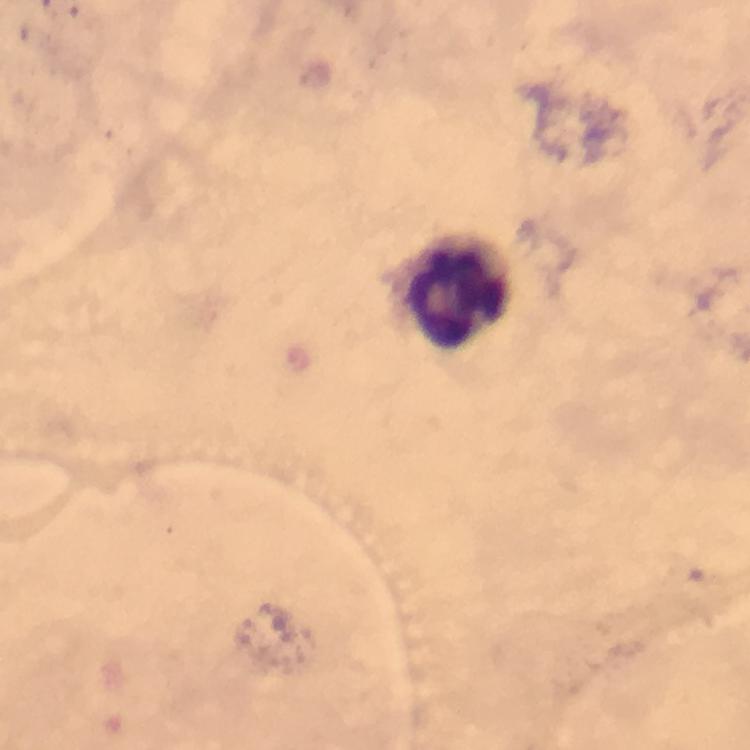
capture: smartphone photograph through a microscope
leukocyte_locations: 'approximate centers as {x, y} in pixels: {455, 292}'
immersion_oil: applied
image_size: 750×750 pixels
cropped_from: a single field of view
preparation: thick smear
context: from a malaria diagnostic workup
magnification: 100x
stain: Giemsa
plasmodium_parasites: none detected